Report the malaria status of this cell.
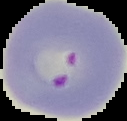

It is parasitized.

image type = segmented cell region on a black background
preparation = thin blood smear
image size = 127×121 pixels